Report the malaria status of this cell.
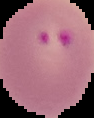

Parasitized.

Cell region segmented out of the field of view; the surrounding area is masked to black. From a thin blood film. Image is 94×118 pixels.